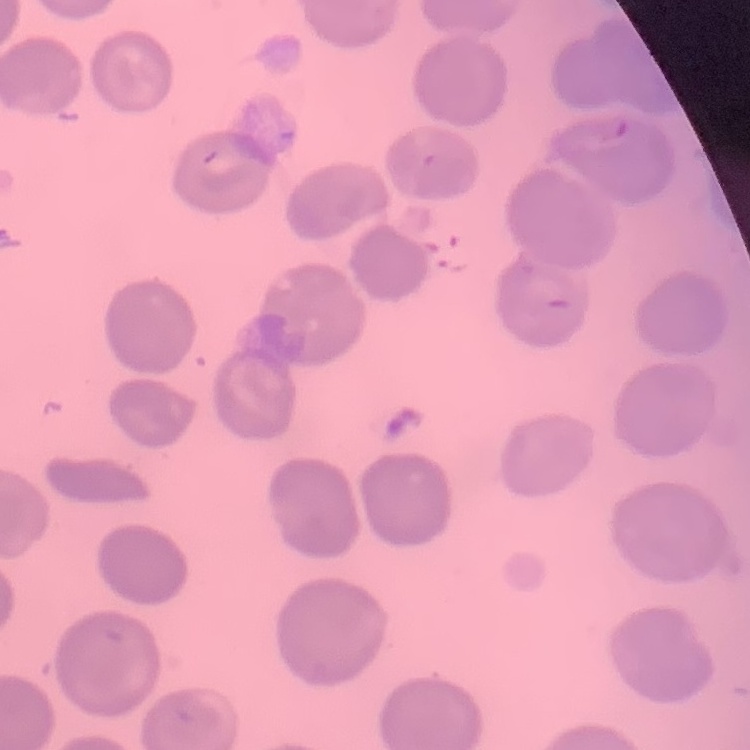
Summary:
  - Erythrocyte morphology: no rouleaux formation
  - Stain: Field's or Giemsa
  - Preparation: thin peripheral smear
  - Image type: one tile cut from a larger photomicrograph